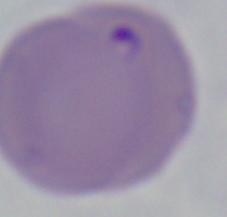
identification = Babesia
magnification = 1000x
modality = photomicrograph